State which parasite is depicted.
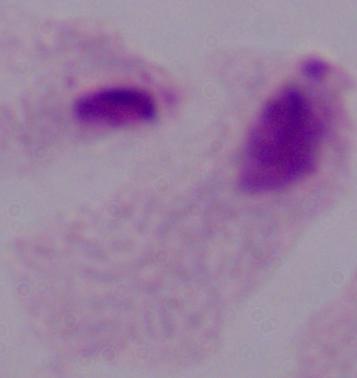

A trichomonad.

modality = micrograph
magnification = 1000x